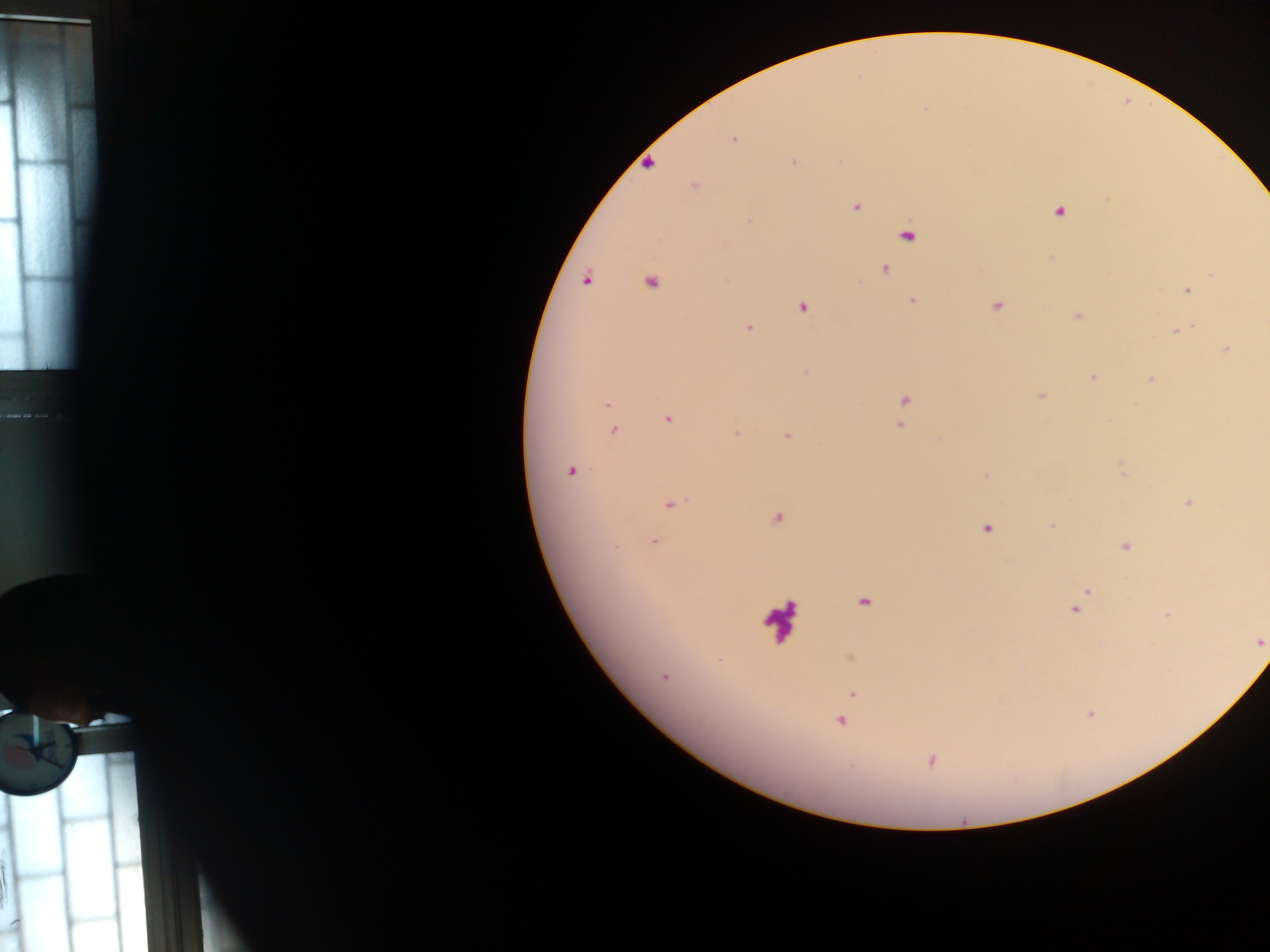

{
  "country": "Ghana",
  "capture": "mobile-phone photograph through a microscope",
  "image_size": "1270×952 pixels",
  "leukocyte_locations": "approximate centers as {x, y} in pixels: {779, 620}",
  "plasmodium_parasite_locations": "approximate centers as {x, y} in pixels: {733, 140}, {793, 161}, {648, 164}, {693, 185}, {1108, 198}, {856, 207}, {1059, 211}, {748, 222}, {907, 235}, {884, 269}, {1213, 274}, {586, 281}, {650, 282}, {1186, 290}, {912, 301}, {996, 306}, {803, 307}, {748, 327}, {1176, 331}, {1226, 350}, {805, 373}, {1093, 377}, {1150, 379}, {1042, 396}, {904, 400}, {607, 404}, {668, 420}, {901, 424}, {614, 430}, {736, 434}, {787, 436}, {1122, 469}, {570, 471}, {986, 477}, {1188, 503}, {671, 504}, {777, 518}, {1051, 525}, {986, 528}, {654, 541}, {1125, 546}, {1086, 592}, {864, 603}, {1076, 609}, {1259, 642}, {664, 677}, {852, 693}, {841, 721}, {932, 760}",
  "preparation": "thick blood film",
  "field_of_view": "single"
}